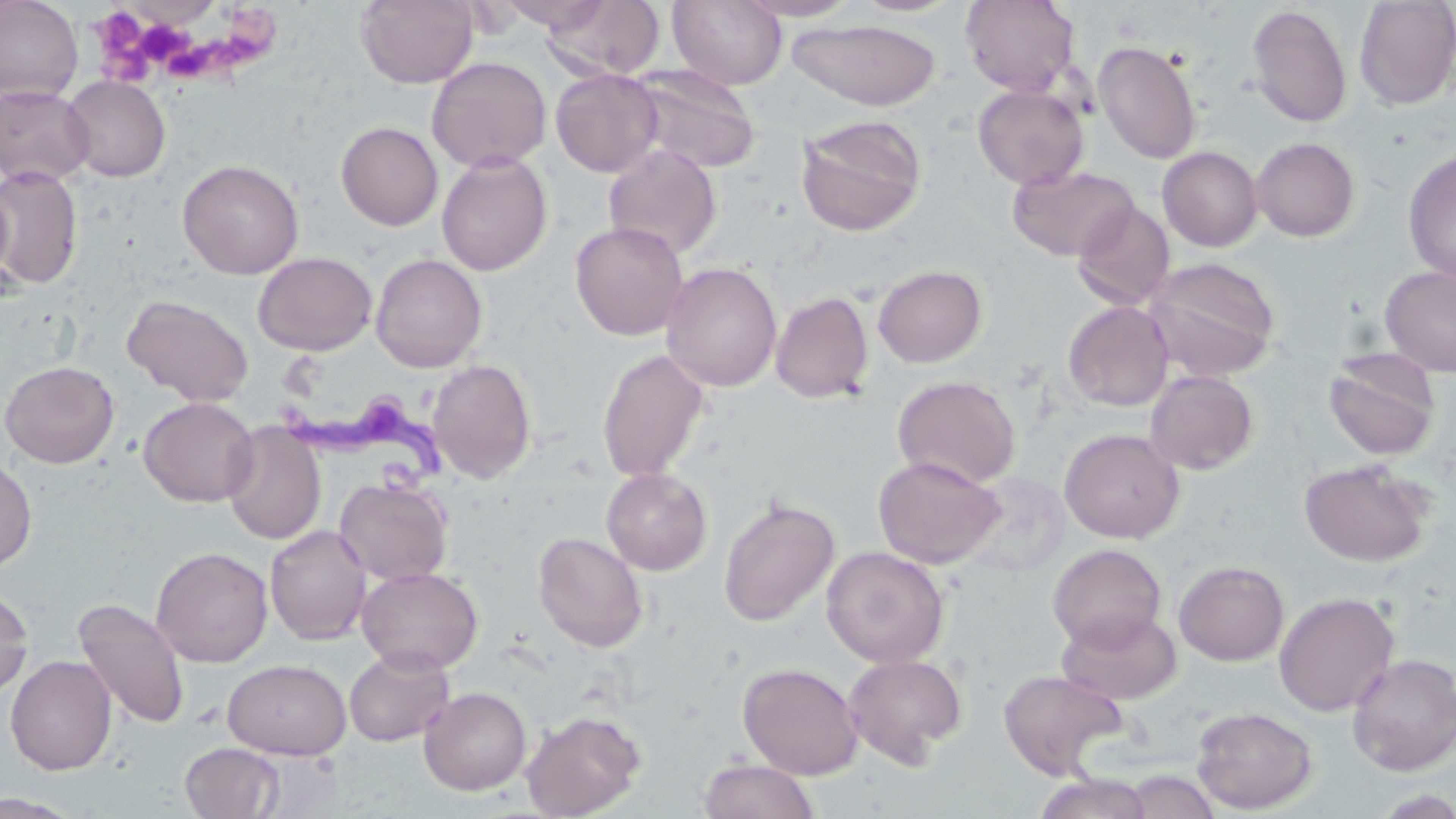
Summary:
  - Coordinate format: approximate bounding boxes as named x1/y1/x2/y2 corners in pixels
  - Platelet locations: (x1=90, y1=10, x2=159, y2=84), (x1=137, y1=22, x2=188, y2=64), (x1=168, y1=47, x2=204, y2=80)
  - Trypanosoma brucei locations: (x1=279, y1=399, x2=456, y2=509)
  - Uninfected red blood cell locations: (x1=0, y1=0, x2=83, y2=105), (x1=355, y1=0, x2=478, y2=88), (x1=500, y1=0, x2=613, y2=34), (x1=541, y1=0, x2=665, y2=81), (x1=667, y1=0, x2=788, y2=90), (x1=734, y1=0, x2=863, y2=21), (x1=852, y1=0, x2=963, y2=17), (x1=960, y1=0, x2=1080, y2=96), (x1=1354, y1=0, x2=1456, y2=111), (x1=1246, y1=5, x2=1352, y2=128), (x1=787, y1=18, x2=943, y2=110), (x1=1093, y1=40, x2=1202, y2=164), (x1=427, y1=56, x2=551, y2=173), (x1=626, y1=63, x2=761, y2=175), (x1=551, y1=68, x2=663, y2=177), (x1=61, y1=75, x2=170, y2=182), (x1=0, y1=84, x2=95, y2=187), (x1=972, y1=84, x2=1089, y2=190), (x1=795, y1=115, x2=927, y2=237), (x1=336, y1=122, x2=443, y2=230), (x1=1251, y1=136, x2=1360, y2=242), (x1=603, y1=144, x2=722, y2=261), (x1=1157, y1=146, x2=1263, y2=252), (x1=1402, y1=150, x2=1456, y2=285), (x1=436, y1=151, x2=552, y2=276), (x1=178, y1=159, x2=305, y2=280), (x1=1, y1=166, x2=83, y2=290), (x1=1007, y1=166, x2=1139, y2=261), (x1=0, y1=179, x2=17, y2=299), (x1=1072, y1=201, x2=1175, y2=310), (x1=570, y1=221, x2=689, y2=341), (x1=253, y1=252, x2=377, y2=355), (x1=370, y1=253, x2=488, y2=373), (x1=1144, y1=257, x2=1280, y2=381), (x1=661, y1=262, x2=782, y2=392), (x1=872, y1=264, x2=987, y2=368), (x1=1379, y1=265, x2=1456, y2=378), (x1=770, y1=291, x2=873, y2=404), (x1=121, y1=294, x2=254, y2=408), (x1=1063, y1=300, x2=1174, y2=412), (x1=1323, y1=347, x2=1442, y2=462), (x1=597, y1=348, x2=710, y2=483), (x1=427, y1=359, x2=537, y2=484), (x1=1, y1=360, x2=120, y2=468), (x1=1144, y1=369, x2=1259, y2=476), (x1=892, y1=375, x2=1021, y2=489), (x1=138, y1=396, x2=259, y2=507), (x1=222, y1=421, x2=326, y2=545), (x1=1060, y1=428, x2=1185, y2=543), (x1=243, y1=435, x2=338, y2=610), (x1=0, y1=455, x2=37, y2=572), (x1=873, y1=455, x2=1005, y2=569), (x1=1298, y1=458, x2=1434, y2=567), (x1=601, y1=468, x2=713, y2=575), (x1=335, y1=477, x2=453, y2=585), (x1=718, y1=496, x2=840, y2=627), (x1=265, y1=524, x2=372, y2=645), (x1=533, y1=531, x2=649, y2=652), (x1=1047, y1=544, x2=1167, y2=652), (x1=821, y1=546, x2=950, y2=668), (x1=150, y1=547, x2=273, y2=667), (x1=1173, y1=560, x2=1289, y2=666), (x1=356, y1=566, x2=483, y2=675), (x1=0, y1=585, x2=33, y2=699), (x1=1273, y1=591, x2=1400, y2=717), (x1=72, y1=597, x2=190, y2=730), (x1=1056, y1=608, x2=1181, y2=705), (x1=344, y1=647, x2=455, y2=747), (x1=841, y1=653, x2=968, y2=768), (x1=1347, y1=653, x2=1456, y2=775), (x1=5, y1=654, x2=117, y2=775), (x1=222, y1=659, x2=352, y2=760), (x1=737, y1=662, x2=864, y2=779), (x1=997, y1=668, x2=1129, y2=779), (x1=418, y1=686, x2=533, y2=795), (x1=1191, y1=706, x2=1317, y2=814), (x1=521, y1=710, x2=647, y2=818), (x1=180, y1=742, x2=286, y2=818), (x1=698, y1=758, x2=820, y2=819), (x1=1122, y1=770, x2=1221, y2=818), (x1=1032, y1=773, x2=1156, y2=819), (x1=0, y1=792, x2=84, y2=818)
  - Slide-level diagnosis: Trypanosoma brucei
  - Modality: light microscopy
  - Magnification: 1000x
  - Image size: 1456×819 pixels
  - Field of view: one of a larger specimen
  - Stain: May-Grünwald-Giemsa
  - Preparation: thin blood film